Name the parasite shown.
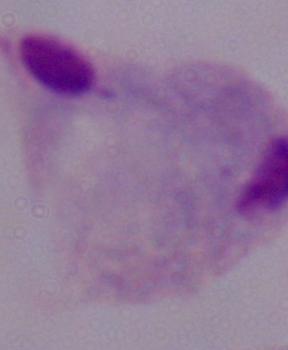

This is a trichomonad.

modality = photomicrograph
magnification = 1000x